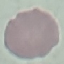
Summary:
  - Result: negative for malaria parasites
  - Stain: Giemsa
  - Capture: smartphone camera at the microscope eyepiece
  - Preparation: thin smear
  - Image type: automatically extracted cell patch, resized to 64 × 64 pixels